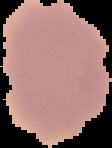

image size = 112×148 pixels
preparation = thin blood film
result = no Plasmodium parasites detected
image type = cell region segmented out of the field of view; surrounding area masked to black